Outline each Babesia divergens-infected red blood cell.
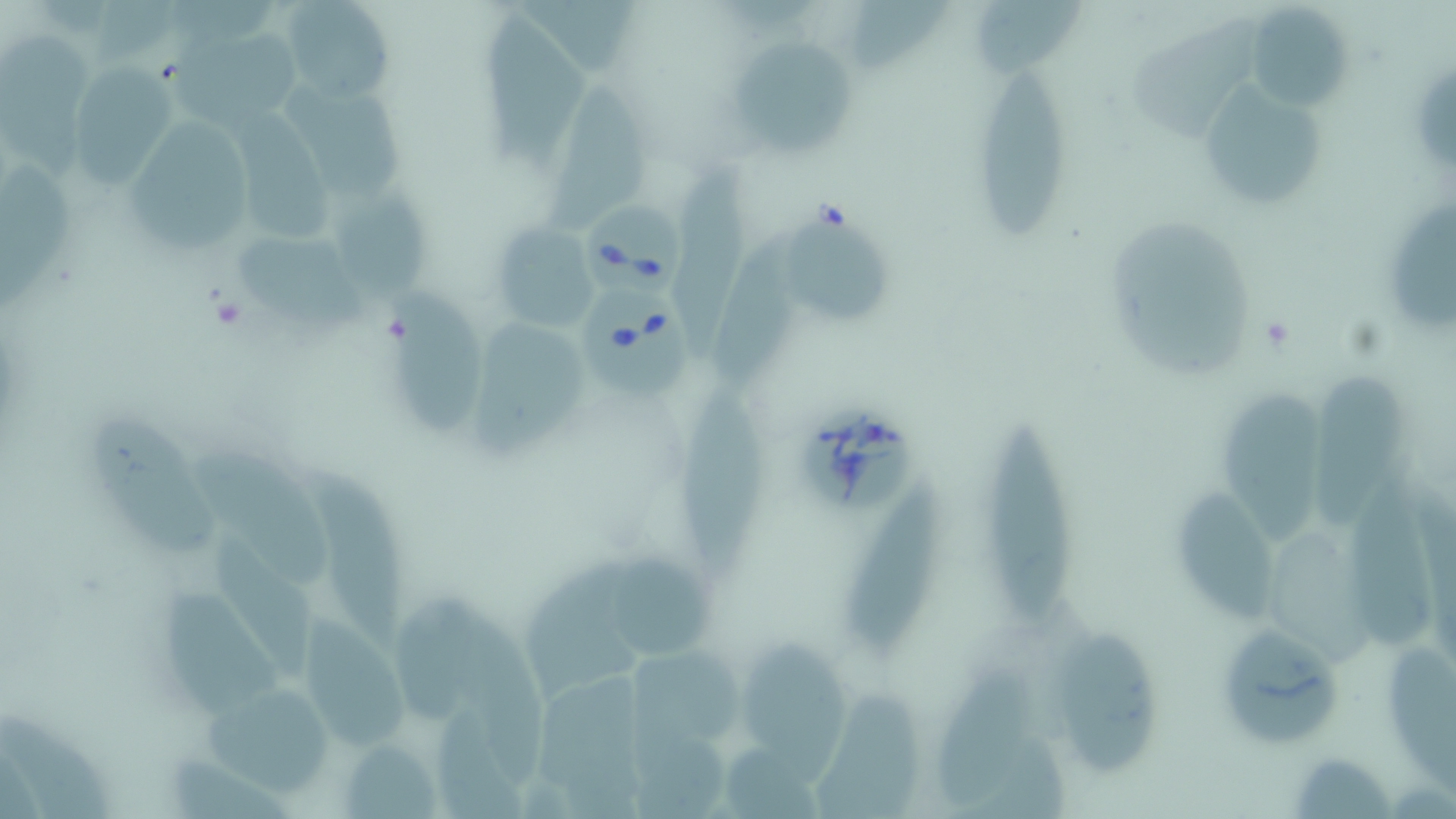
Approximate bounding boxes as named x1/y1/x2/y2 corners in pixels.
Babesia divergens-infected red blood cells: (x1=584, y1=194, x2=685, y2=303), (x1=579, y1=284, x2=694, y2=402), (x1=789, y1=403, x2=919, y2=521).

{
  "slide_level_diagnosis": "Babesia divergens",
  "field_of_view": "one of a larger specimen",
  "stain": "May-Grünwald-Giemsa",
  "preparation": "thin blood film",
  "image_size": "1456×819 pixels",
  "magnification": "1000x",
  "modality": "optical microscopy",
  "uninfected_red_blood_cell_locations": "approximate bounding boxes as named x1/y1/x2/y2 corners in pixels: (x1=279, y1=0, x2=398, y2=102), (x1=846, y1=1, x2=949, y2=69), (x1=976, y1=2, x2=1089, y2=79), (x1=1244, y1=4, x2=1353, y2=110), (x1=1128, y1=8, x2=1259, y2=148), (x1=477, y1=13, x2=593, y2=172), (x1=0, y1=26, x2=94, y2=176), (x1=171, y1=33, x2=305, y2=138), (x1=726, y1=35, x2=853, y2=159), (x1=67, y1=62, x2=179, y2=189), (x1=1407, y1=64, x2=1453, y2=172), (x1=972, y1=70, x2=1071, y2=239), (x1=1196, y1=77, x2=1328, y2=219), (x1=282, y1=80, x2=414, y2=199), (x1=544, y1=82, x2=656, y2=233), (x1=233, y1=97, x2=335, y2=243), (x1=124, y1=110, x2=260, y2=252), (x1=673, y1=159, x2=748, y2=358), (x1=0, y1=162, x2=74, y2=307), (x1=334, y1=185, x2=428, y2=298), (x1=1392, y1=198, x2=1456, y2=337), (x1=786, y1=206, x2=900, y2=329), (x1=1111, y1=213, x2=1254, y2=378), (x1=490, y1=222, x2=600, y2=332), (x1=238, y1=231, x2=373, y2=331), (x1=714, y1=235, x2=816, y2=385), (x1=385, y1=286, x2=489, y2=438), (x1=466, y1=319, x2=594, y2=458), (x1=1311, y1=367, x2=1409, y2=532), (x1=675, y1=377, x2=763, y2=591), (x1=1220, y1=383, x2=1330, y2=546), (x1=985, y1=407, x2=1075, y2=630), (x1=84, y1=411, x2=218, y2=556), (x1=189, y1=445, x2=328, y2=585), (x1=305, y1=458, x2=402, y2=661), (x1=848, y1=474, x2=949, y2=658), (x1=1352, y1=475, x2=1436, y2=655), (x1=1174, y1=491, x2=1283, y2=627), (x1=213, y1=533, x2=324, y2=685), (x1=1274, y1=533, x2=1372, y2=671), (x1=607, y1=554, x2=712, y2=664), (x1=519, y1=562, x2=649, y2=700), (x1=163, y1=586, x2=289, y2=716), (x1=391, y1=588, x2=491, y2=722), (x1=300, y1=614, x2=406, y2=749), (x1=466, y1=614, x2=539, y2=785), (x1=1230, y1=624, x2=1337, y2=742), (x1=738, y1=630, x2=850, y2=783), (x1=1060, y1=632, x2=1161, y2=778), (x1=630, y1=638, x2=748, y2=748), (x1=1388, y1=642, x2=1456, y2=792), (x1=932, y1=661, x2=1036, y2=807), (x1=541, y1=663, x2=641, y2=816), (x1=196, y1=687, x2=343, y2=793), (x1=811, y1=691, x2=920, y2=817), (x1=1, y1=709, x2=114, y2=819), (x1=630, y1=717, x2=739, y2=819), (x1=724, y1=736, x2=827, y2=819), (x1=342, y1=738, x2=442, y2=817), (x1=1295, y1=754, x2=1396, y2=818)"
}